Outline each blood parasite and name the species.
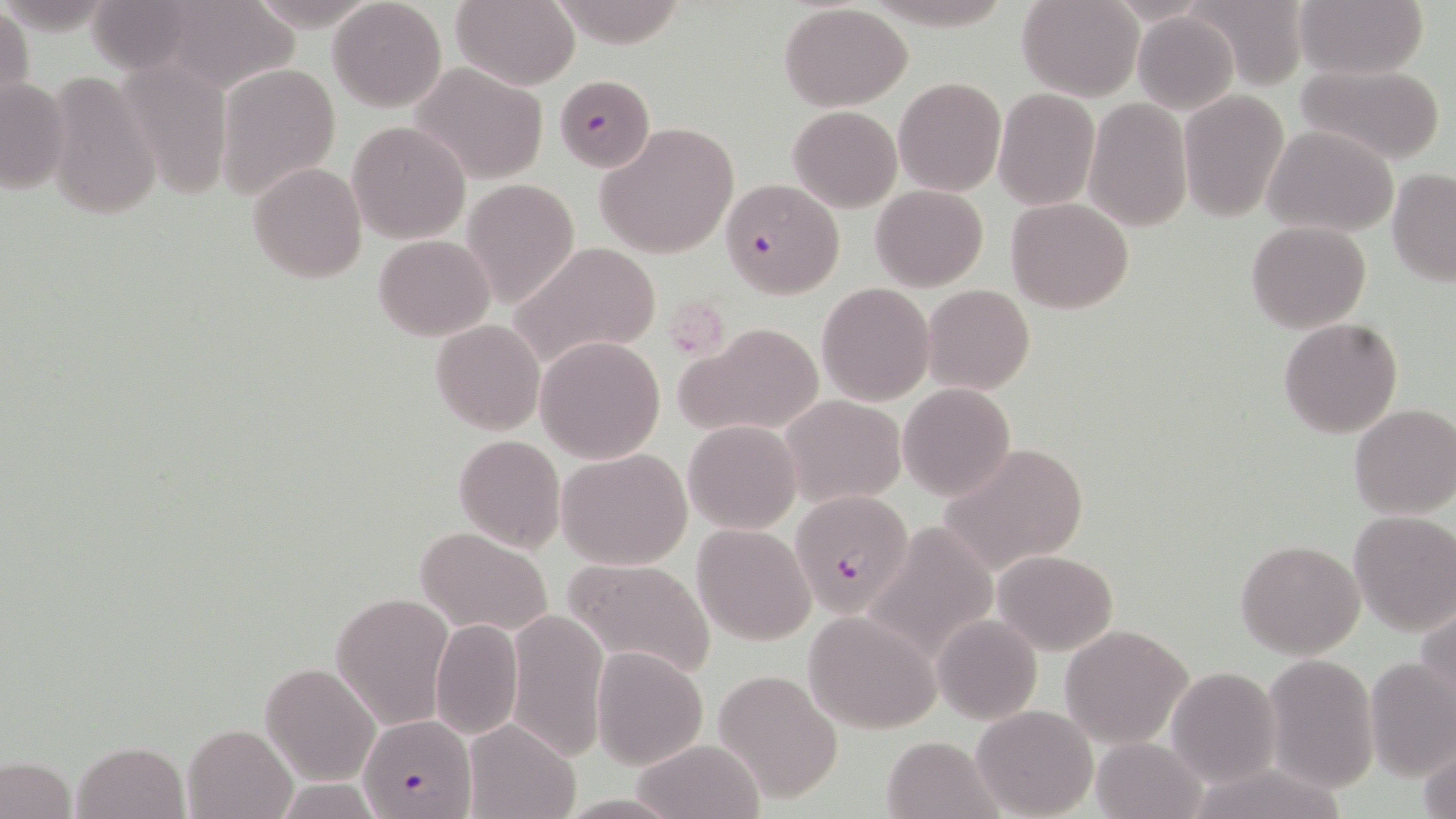
Approximate bounding boxes as [x1, y1, x2, y2] in pixels.
Plasmodium falciparum-infected red blood cells: [555, 75, 653, 172], [720, 178, 843, 300], [791, 492, 911, 616], [362, 714, 476, 819].
No Plasmodium ovale, Plasmodium malariae, Plasmodium vivax, Babesia divergens, or Trypanosoma brucei observed.

Platelet locations: [672, 297, 728, 365]. Uninfected red blood cell locations: [327, 0, 447, 113], [452, 0, 581, 90], [1017, 0, 1144, 101], [1185, 0, 1312, 89], [1295, 0, 1426, 79], [154, 1, 300, 94], [84, 2, 210, 75], [779, 4, 913, 110], [0, 8, 34, 118], [1132, 12, 1240, 114], [114, 59, 234, 200], [409, 61, 551, 185], [218, 62, 342, 199], [1296, 63, 1448, 164], [43, 71, 162, 221], [893, 76, 1006, 197], [0, 78, 71, 194], [993, 90, 1099, 210], [1179, 92, 1289, 222], [1083, 100, 1191, 230], [789, 106, 902, 212], [348, 121, 469, 244], [595, 122, 739, 259], [1265, 125, 1399, 236], [247, 162, 367, 283], [1387, 169, 1456, 285], [461, 178, 580, 310], [871, 184, 988, 291], [1007, 198, 1132, 314], [1245, 221, 1372, 334], [373, 234, 493, 341], [510, 241, 663, 370], [816, 282, 935, 405], [923, 284, 1035, 395], [1279, 318, 1403, 438], [431, 319, 545, 435], [683, 322, 827, 438], [536, 336, 666, 462], [898, 384, 1015, 501], [781, 396, 906, 507], [1349, 403, 1456, 518], [684, 419, 801, 534], [454, 434, 566, 554], [936, 443, 1088, 575], [558, 448, 693, 570], [1348, 510, 1456, 635], [863, 521, 1003, 661], [692, 525, 814, 644], [414, 526, 555, 639], [1235, 538, 1366, 659], [992, 549, 1117, 657], [564, 558, 718, 682], [331, 592, 453, 729], [1418, 604, 1456, 718], [505, 608, 609, 764], [803, 609, 942, 734], [934, 614, 1041, 724], [429, 618, 524, 740], [1059, 625, 1193, 747], [591, 647, 708, 769], [1263, 653, 1379, 792], [1363, 657, 1455, 782], [260, 663, 379, 785], [1168, 667, 1280, 786], [714, 670, 842, 803], [971, 704, 1096, 818], [463, 719, 579, 819], [183, 725, 296, 818], [880, 734, 1002, 819], [1416, 736, 1456, 819], [632, 737, 765, 819], [1091, 737, 1208, 818], [71, 741, 191, 819], [0, 754, 77, 819]. Slide-level diagnosis: Plasmodium falciparum. Image is 1456×819 pixels. May-Grünwald-Giemsa stain. Thin blood film. Light microscopy. Single field of view. 1000x magnification.